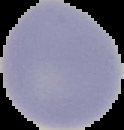

Image is 124×130 pixels. From a thin blood film. Cell region segmented out of the field of view; the surrounding area is masked to black. Result: no Plasmodium parasites detected.